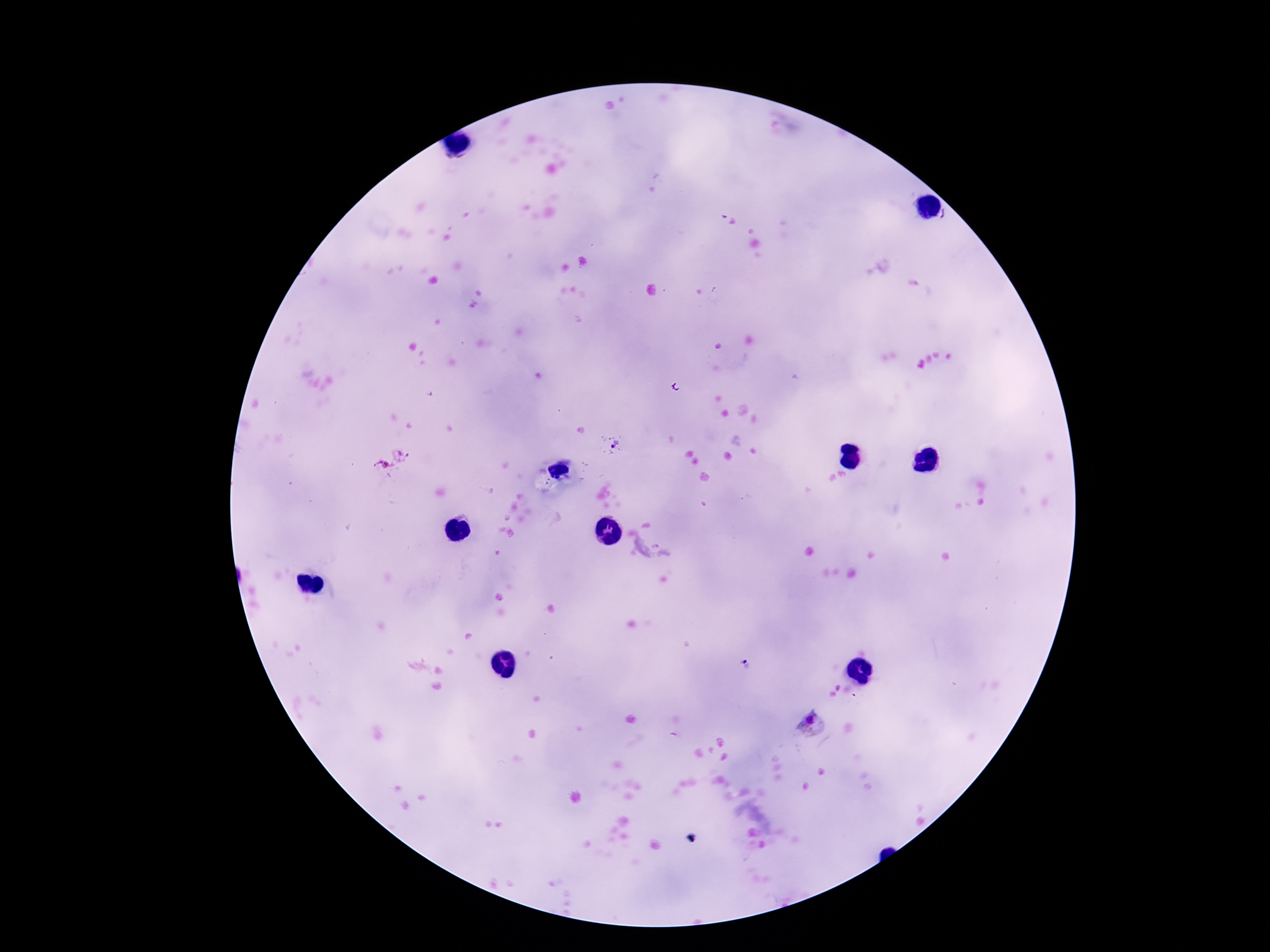

Approximate object centers, in pixels from the top-left corner.
Summary:
  - Plasmodium parasite locations: (x=612, y=443), (x=385, y=468), (x=746, y=665), (x=814, y=723)
  - Preparation: thick blood smear
  - Capture: smartphone camera through the microscope eyepiece
  - Field of view: single
  - Image size: 1270×952 pixels
  - Patient malaria status: infected
  - Stain: Giemsa
  - Magnification: 100x